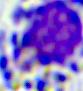
modality = micrograph
identification = leukocyte
magnification = 400x